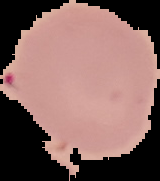
preparation = thin blood smear
malaria status = uninfected
image size = 160×181 pixels
image type = segmented cell region with the area outside set to black